Comment on the morphology of the red blood cells.
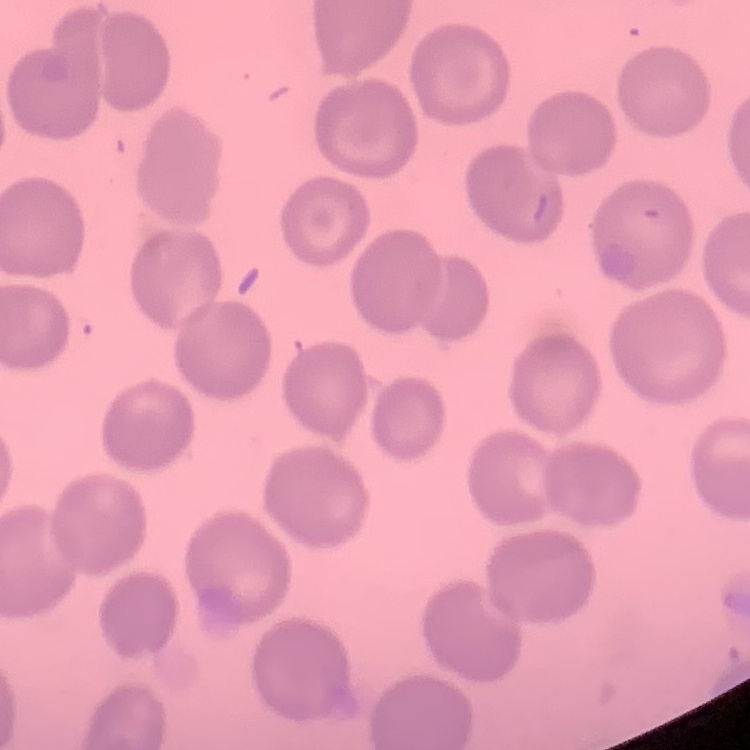

No rouleaux formation.

Summary:
  - Stain: Field's or Giemsa
  - Preparation: thin peripheral smear
  - Image type: square crop of a larger photomicrograph